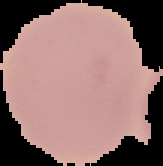

Summary:
  - Image size: 163×166 pixels
  - Image type: segmented cell region with the area outside set to black
  - Preparation: thin blood smear
  - Malaria status: uninfected